Assess this cell for malaria.
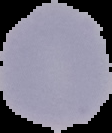

It is uninfected.

Image is 112×133 pixels. From a thin blood smear. Segmented cell region on a black background.